Identify the parasite.
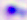
This is Toxoplasma gondii.

Summary:
  - Magnification: 400x
  - Modality: micrograph